Classify this cell by malaria status.
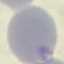
It is uninfected.

Summary:
  - Preparation: thin blood film
  - Stain: Giemsa
  - Capture: smartphone camera at the microscope eyepiece
  - Image type: automatically extracted cell patch, resized to 64 × 64 pixels